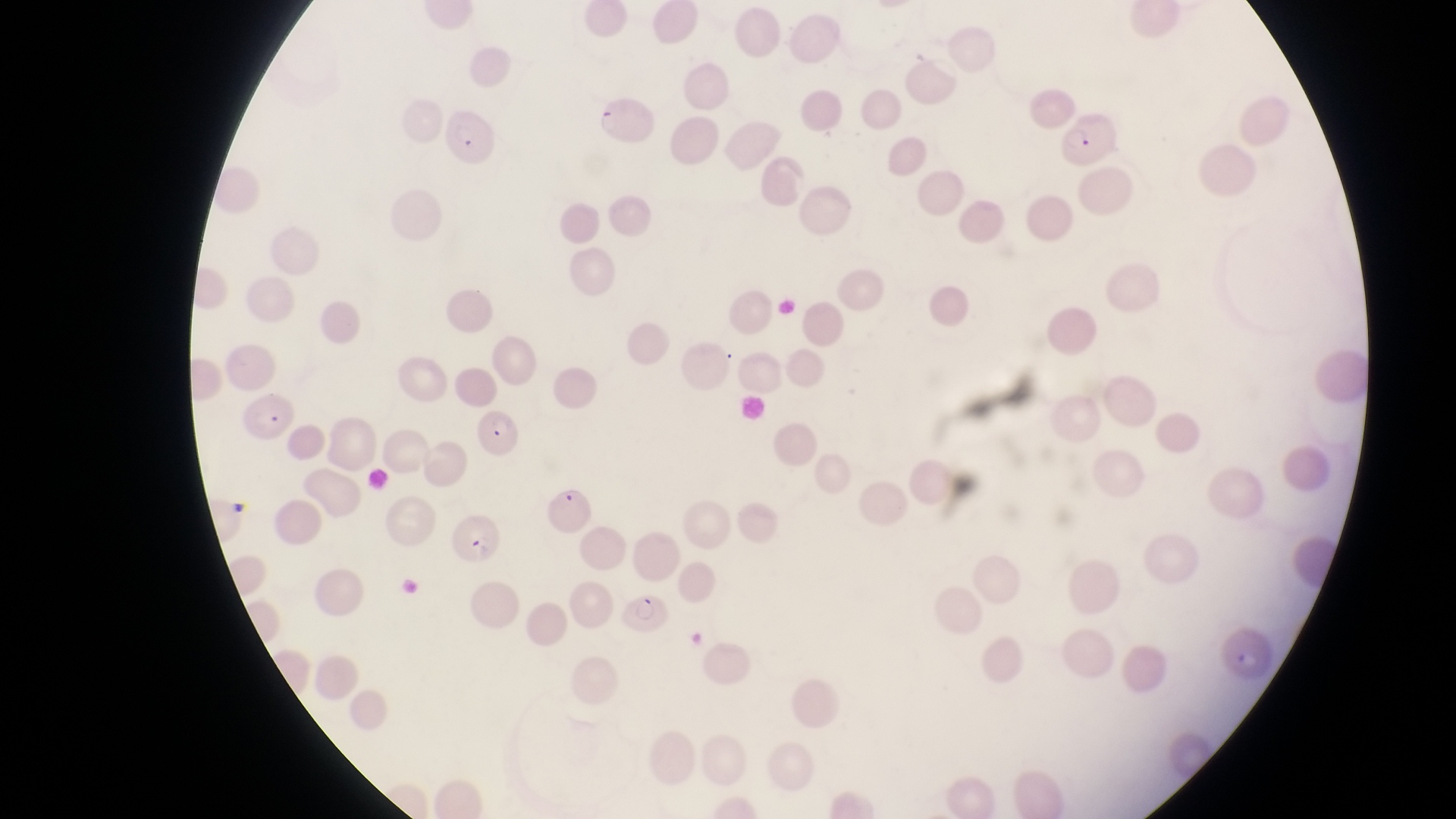
Approximate bounding boxes as {left, top, right, bottom} in pixels.
Summary:
  - Parasitised red blood cell locations: {597, 96, 654, 150}, {1062, 103, 1109, 164}, {439, 106, 500, 170}, {240, 393, 303, 442}, {470, 415, 526, 457}, {532, 476, 596, 536}, {450, 505, 503, 563}, {620, 592, 676, 638}
  - Image size: 1456×819 pixels
  - Country: Uganda
  - Magnification: 1000x
  - Preparation: thin blood smear
  - Capture: smartphone photograph through the eyepiece of an Olympus CX-23 microscope
  - Field of view: single